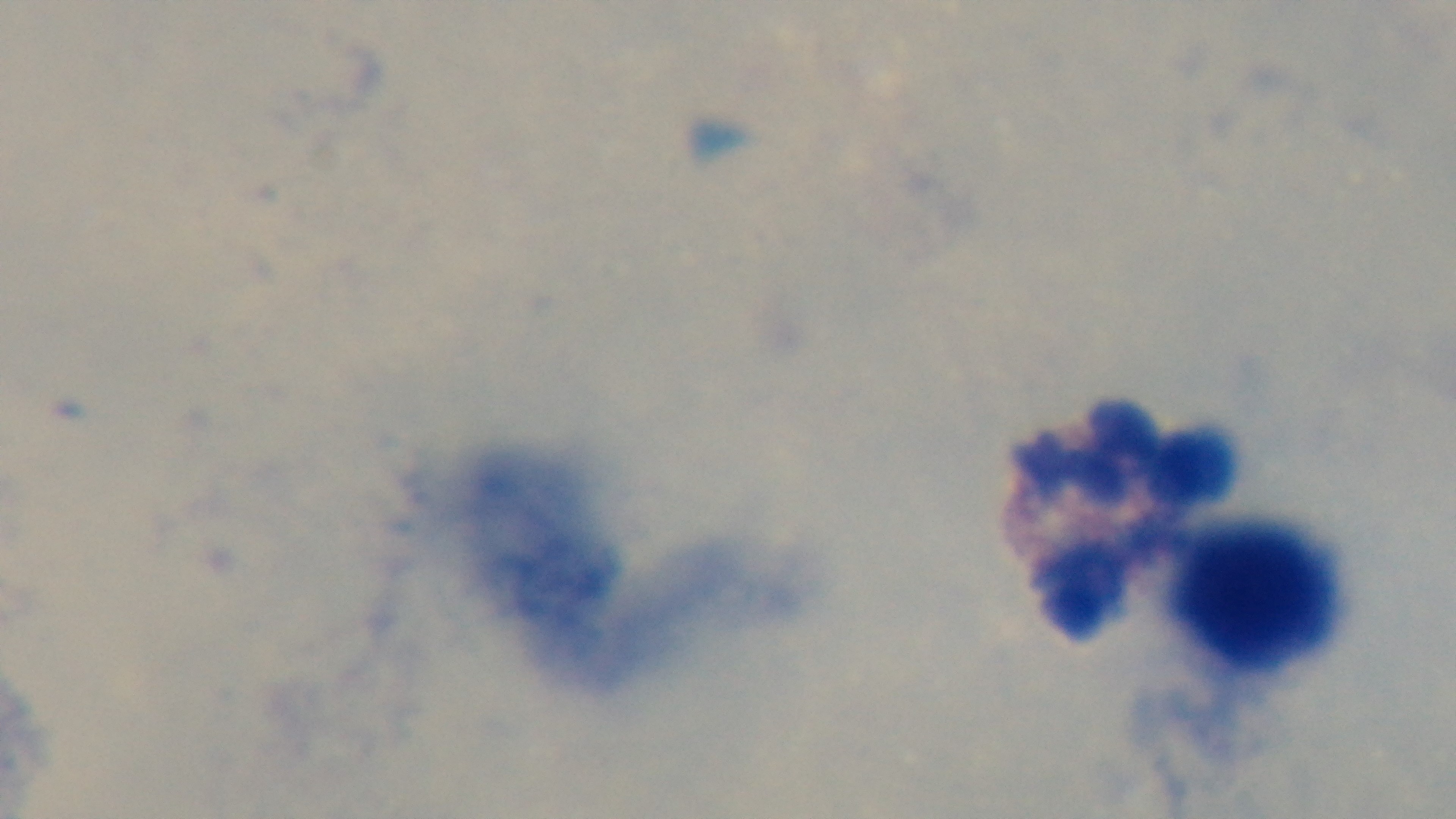

Preparation: thick. Light microscopy. Single field of view. Oil-immersion objective, 100x. Giemsa-stained. Malaria status: uninfected. Captured with a mounted 4K digital camera.